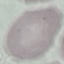

Result: no malaria parasites detected. Thin blood smear. Cell patch, automatically extracted from a larger field of view and resized to 64 × 64 pixels. Photographed with a smartphone camera at the microscope eyepiece. Giemsa-stained preparation.